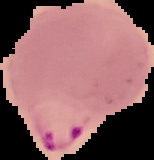

Summary:
  - Image size: 154×160 pixels
  - Preparation: thin blood smear
  - Result: malaria parasites detected
  - Image type: segmented cell region with the area outside set to black